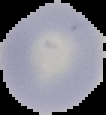
Summary:
  - Malaria status: uninfected
  - Image type: segmented cell region on a black background
  - Image size: 106×115 pixels
  - Preparation: thin blood film